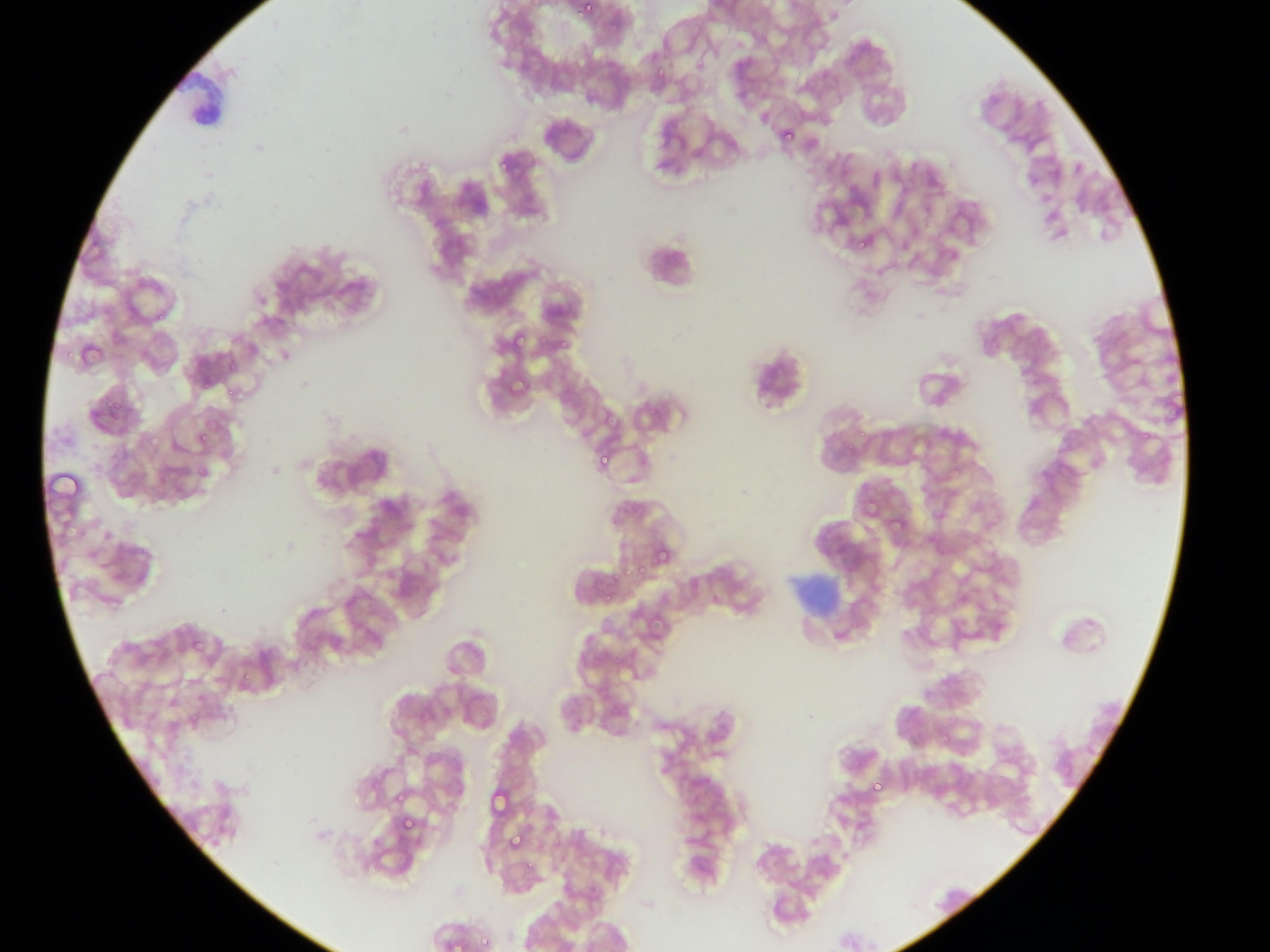
leukocyte locations = approximate bounding boxes as [left, top, right, bottom] in pixels: [638, 228, 705, 294]
country = Ghana
malaria parasite locations = approximate bounding boxes as [left, top, right, bottom] in pixels: [579, 1, 595, 17], [777, 128, 799, 142], [1071, 162, 1083, 176], [505, 337, 535, 344], [502, 370, 529, 397], [195, 430, 208, 445], [597, 448, 611, 469], [889, 514, 905, 531], [651, 545, 671, 565], [863, 777, 887, 796], [487, 789, 503, 820], [399, 812, 414, 833], [507, 833, 524, 851], [476, 926, 488, 950]
image size = 1270×952 pixels
preparation = thin blood smear
capture = mobile-phone photograph through a microscope
field of view = single